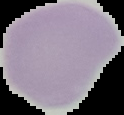 Image is 124×115 pixels. From a thin blood smear. Cell region segmented out of the field of view; the surrounding area is masked to black. Malaria status: uninfected.